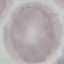 Result: no malaria parasites seen. Cell patch, automatically extracted from a larger field of view and resized to 64 × 64 pixels. Giemsa stain. Thin smear of blood. Acquired by smartphone through the microscope eyepiece.